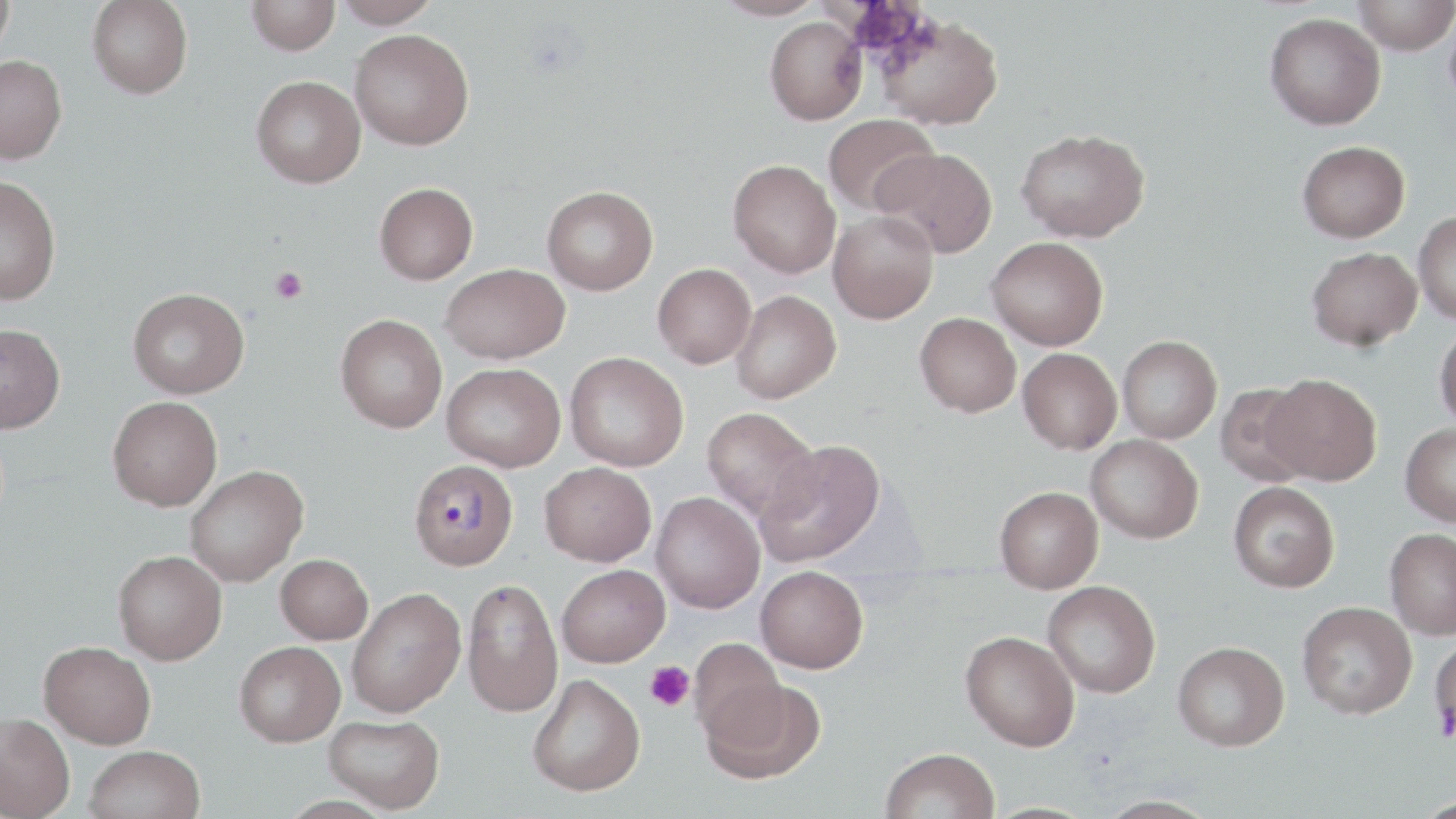
Approximate bounding boxes as [x1, y1, x2, y2] in pixels. Platelet locations: [269, 267, 308, 305], [644, 661, 695, 711]. Plasmodium malariae-infected red blood cell locations: [408, 459, 518, 571]. Uninfected red blood cell locations: [0, 0, 16, 59], [87, 0, 193, 99], [246, 0, 340, 55], [334, 0, 442, 28], [711, 0, 827, 20], [1352, 0, 1456, 54], [1445, 3, 1456, 110], [1264, 12, 1385, 130], [875, 13, 1004, 130], [764, 17, 867, 125], [349, 29, 474, 150], [0, 54, 67, 165], [251, 75, 366, 188], [823, 114, 939, 215], [1016, 128, 1150, 243], [1298, 140, 1410, 243], [875, 147, 998, 258], [728, 160, 840, 278], [0, 175, 62, 305], [374, 182, 478, 284], [542, 185, 658, 295], [828, 210, 939, 323], [1414, 211, 1456, 325], [986, 236, 1108, 350], [1307, 246, 1422, 351], [440, 263, 569, 363], [653, 263, 756, 368], [128, 287, 249, 398], [731, 290, 841, 403], [915, 312, 1021, 417], [335, 314, 447, 433], [0, 323, 65, 434], [1434, 324, 1456, 430], [1117, 335, 1222, 443], [1018, 347, 1122, 453], [564, 352, 689, 472], [442, 362, 565, 471], [1263, 373, 1382, 485], [1214, 383, 1317, 487], [108, 396, 222, 510], [702, 407, 820, 522], [1400, 423, 1456, 527], [1086, 434, 1203, 543], [757, 440, 885, 567], [539, 461, 655, 566], [185, 465, 308, 586], [1228, 481, 1340, 592], [994, 486, 1103, 592], [651, 492, 765, 613], [1384, 528, 1456, 640], [113, 550, 227, 665], [275, 553, 373, 644], [557, 564, 670, 667], [756, 565, 868, 673], [461, 577, 563, 718], [1042, 580, 1161, 698], [346, 587, 465, 717], [1297, 601, 1417, 719], [961, 630, 1080, 751], [1429, 634, 1456, 747], [689, 636, 786, 742], [234, 640, 346, 746], [40, 641, 156, 748], [1173, 641, 1290, 750], [528, 674, 645, 796], [700, 676, 826, 784], [0, 712, 74, 819], [324, 713, 445, 813], [85, 745, 206, 819], [880, 748, 1000, 819], [1094, 795, 1222, 819]. Slide-level diagnosis: Plasmodium malariae. May-Grünwald-Giemsa-stained preparation. One field of a larger specimen. Image is 1456×819 pixels. Thin blood film. Optical microscopy. 1000x magnification.